State which parasite is depicted.
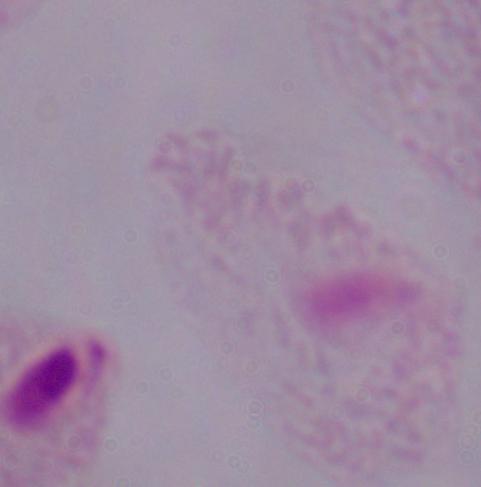
This is a trichomonad.

1000x magnification. Micrograph.